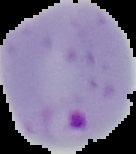
Summary:
  - Preparation: thin blood smear
  - Malaria status: parasitized
  - Image size: 136×154 pixels
  - Image type: segmented cell region on a black background